State which parasite is depicted.
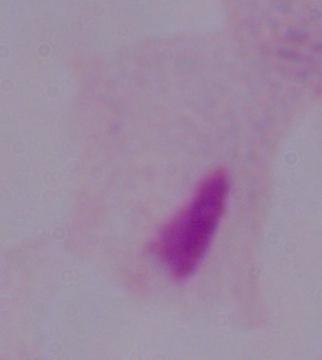

A trichomonad.

Micrograph. 1000x magnification.